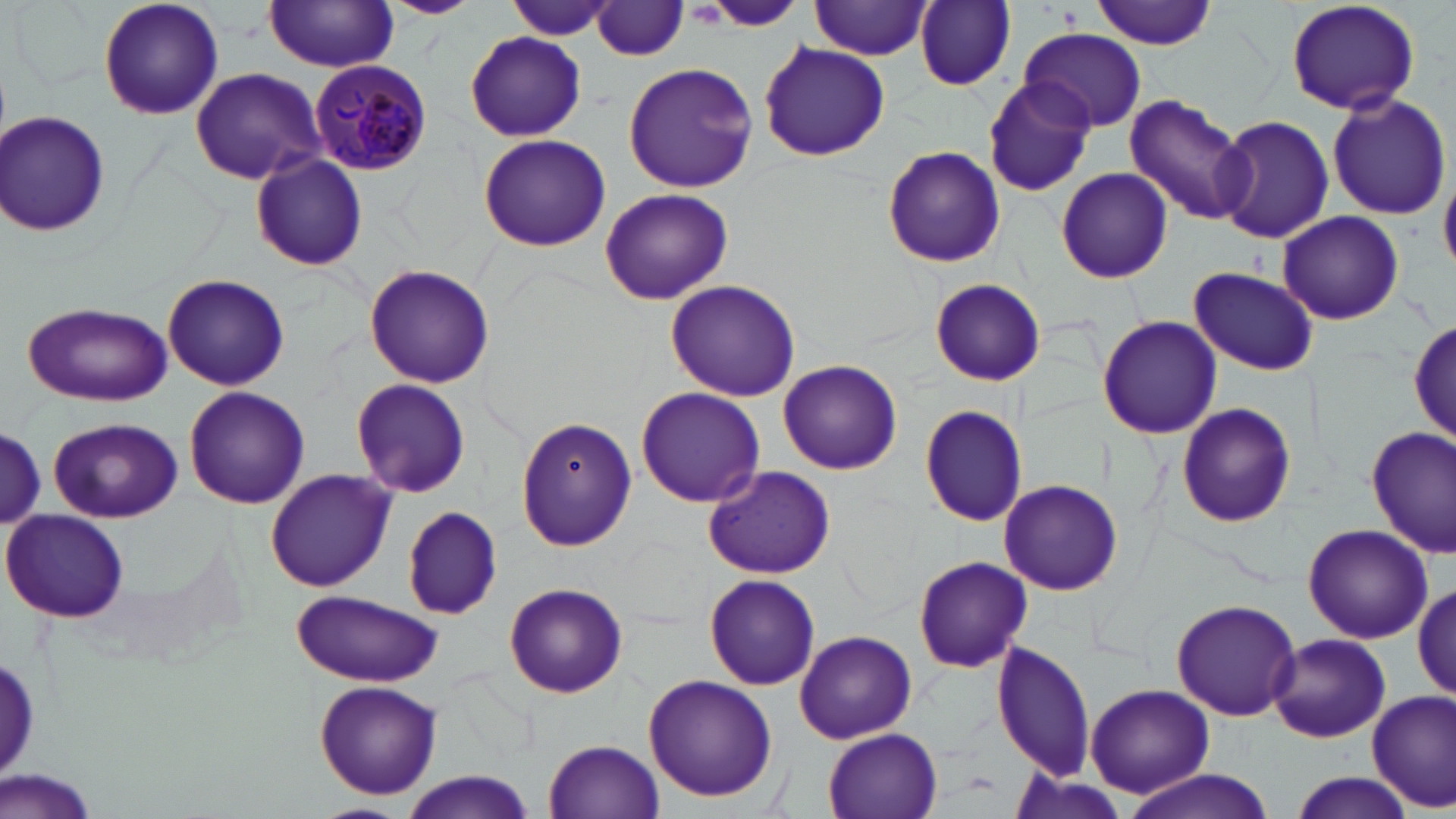
Approximate bounding boxes as [x1, y1, x2, y2] in pixels. Uninfected red blood cell locations: [97, 0, 225, 120], [379, 0, 482, 18], [503, 0, 617, 42], [705, 0, 804, 30], [1093, 0, 1216, 49], [1283, 0, 1422, 116], [810, 1, 932, 60], [593, 2, 690, 60], [916, 2, 1016, 89], [264, 3, 400, 72], [1021, 30, 1146, 132], [465, 32, 588, 142], [759, 41, 890, 162], [622, 60, 759, 192], [189, 67, 329, 185], [983, 76, 1096, 196], [1326, 91, 1450, 220], [1124, 96, 1252, 225], [2, 109, 112, 240], [1210, 115, 1334, 244], [479, 133, 612, 250], [882, 143, 1006, 268], [250, 153, 368, 271], [1441, 164, 1456, 274], [1055, 169, 1173, 284], [598, 187, 733, 305], [1278, 211, 1404, 325], [364, 264, 494, 389], [1190, 266, 1319, 375], [161, 274, 290, 391], [929, 278, 1045, 386], [664, 279, 802, 402], [23, 303, 172, 406], [1097, 315, 1222, 440], [1410, 316, 1456, 447], [778, 360, 902, 473], [350, 377, 472, 499], [184, 387, 309, 509], [636, 387, 766, 507], [1175, 402, 1298, 528], [918, 404, 1027, 527], [50, 417, 182, 524], [517, 418, 636, 552], [1366, 424, 1455, 558], [0, 430, 45, 527], [703, 464, 837, 580], [264, 468, 398, 593], [999, 479, 1124, 597], [403, 506, 501, 619], [3, 508, 129, 623], [1302, 522, 1433, 645], [913, 555, 1032, 673], [704, 575, 822, 689], [504, 581, 629, 698], [1413, 581, 1455, 702], [291, 590, 442, 688], [1169, 598, 1301, 721], [795, 630, 917, 744], [1268, 634, 1391, 745], [991, 639, 1097, 781], [643, 674, 778, 802], [314, 680, 443, 799], [1086, 683, 1217, 798], [1367, 690, 1456, 811], [821, 726, 946, 819], [542, 739, 665, 818], [0, 771, 108, 819], [1116, 771, 1278, 819], [400, 772, 534, 819], [1286, 772, 1418, 819], [307, 802, 413, 819]. Plasmodium malariae-infected red blood cell locations: [309, 60, 432, 173]. Slide-level diagnosis: Plasmodium malariae. Single field of view. Image is 1456×819 pixels. 1000x magnification. Thin blood film. Light microscopy. May-Grünwald-Giemsa-stained preparation.